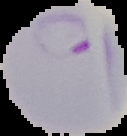
Summary:
  - Image size: 127×136 pixels
  - Preparation: thin blood film
  - Image type: cell region segmented out of the field of view; surrounding area masked to black
  - Result: malaria parasites identified